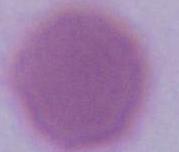 1000x magnification. Photomicrograph. A red blood cell is seen.